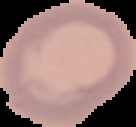

Summary:
  - Image size: 136×127 pixels
  - Preparation: thin blood smear
  - Image type: segmented cell region with the area outside set to black
  - Result: no Plasmodium parasites seen